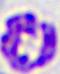
modality: micrograph
identification: white blood cell
magnification: 400x